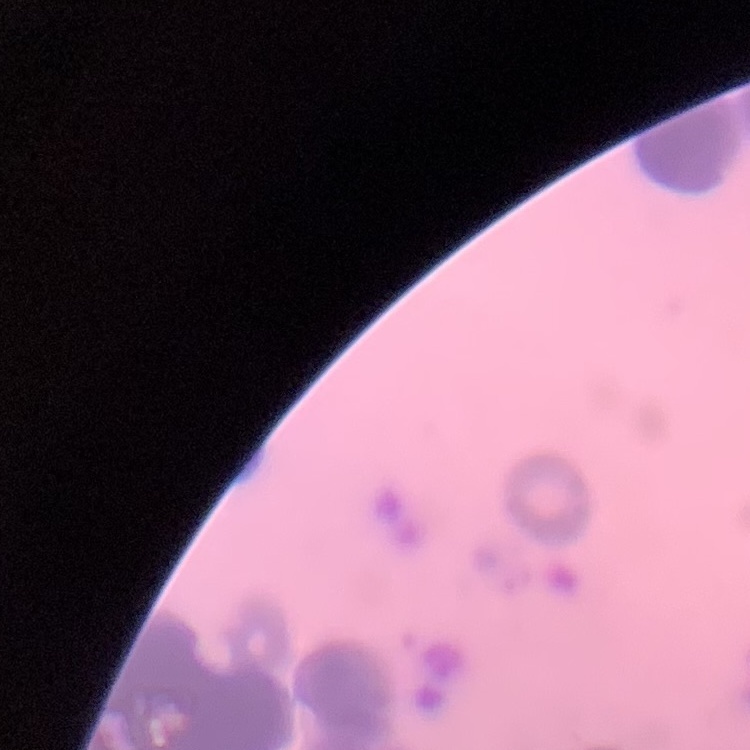
Summary:
  - Red blood cell morphology: rouleaux formation
  - Preparation: thin blood film
  - Stain: Field's or Giemsa
  - Image type: one tile cut from a larger photomicrograph